Locate every Plasmodium ovale-infected red blood cell.
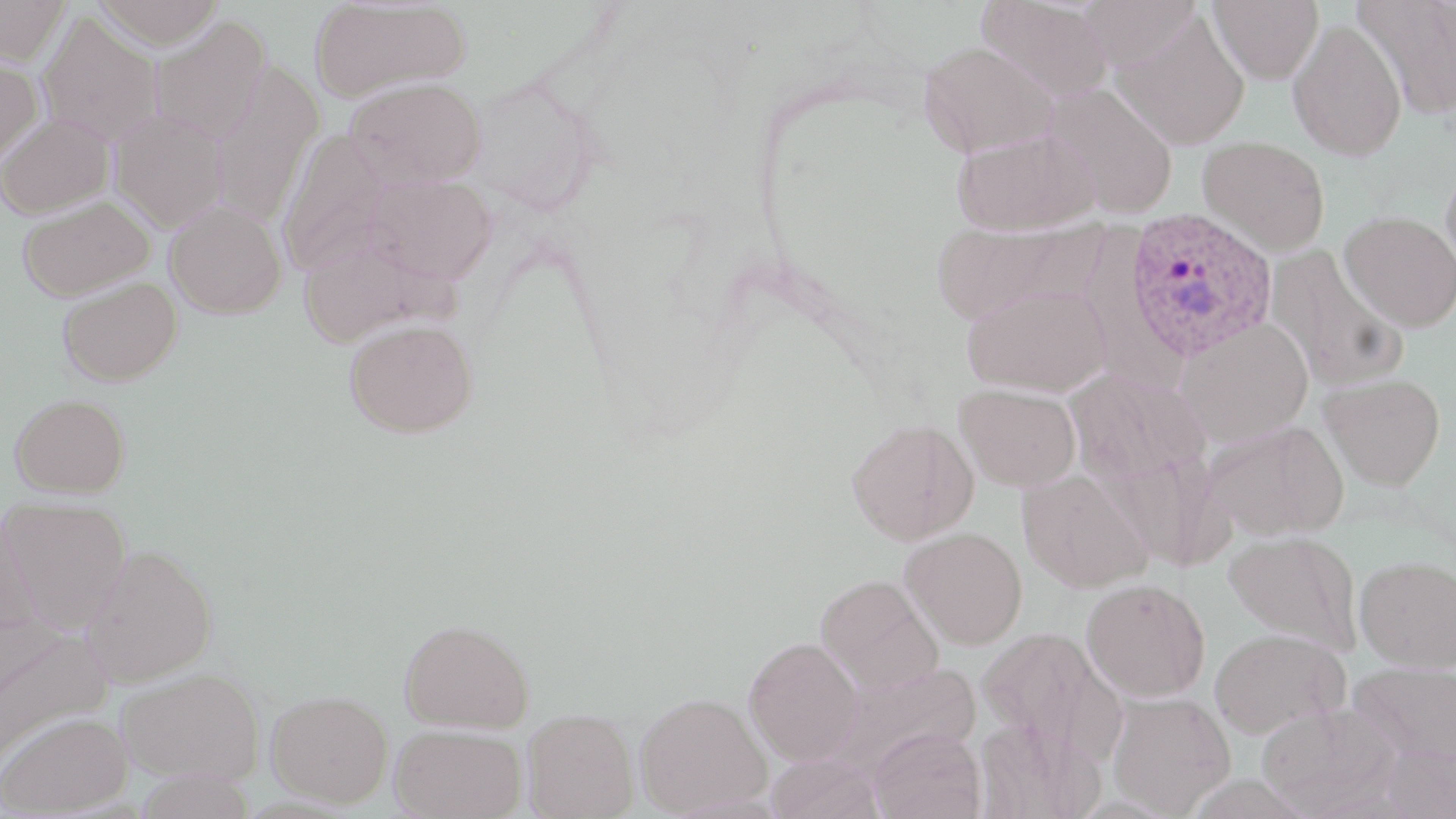
Approximate bounding boxes as (x1, y1, x2, y2) in pixels.
Plasmodium ovale-infected red blood cells: (1123, 207, 1277, 361).

Summary:
  - Uninfected red blood cell locations: (1, 0, 71, 66), (93, 0, 224, 49), (310, 0, 470, 103), (975, 0, 1114, 102), (1209, 0, 1324, 84), (1353, 0, 1456, 121), (1079, 1, 1203, 72), (1111, 10, 1250, 150), (39, 11, 162, 146), (148, 15, 271, 145), (1287, 19, 1407, 161), (918, 40, 1057, 157), (0, 57, 43, 166), (208, 61, 323, 228), (466, 76, 599, 215), (346, 77, 486, 188), (1043, 83, 1179, 219), (111, 108, 228, 233), (0, 113, 114, 219), (277, 128, 391, 276), (952, 128, 1099, 236), (1198, 136, 1330, 255), (1441, 154, 1456, 284), (366, 173, 498, 284), (17, 195, 154, 301), (165, 199, 287, 318), (1340, 211, 1456, 331), (931, 218, 1108, 325), (297, 231, 455, 348), (1267, 245, 1407, 392), (58, 277, 182, 386), (962, 283, 1110, 398), (1175, 317, 1313, 446), (344, 318, 478, 438), (1066, 367, 1212, 496), (1319, 373, 1446, 490), (955, 383, 1081, 491), (10, 394, 130, 497), (846, 418, 979, 545), (1203, 418, 1349, 541), (1018, 469, 1153, 592), (1, 497, 132, 631), (0, 505, 41, 636), (900, 527, 1027, 649), (1224, 530, 1362, 654), (82, 544, 217, 688), (1354, 555, 1456, 672), (815, 575, 943, 696), (1081, 578, 1210, 701), (400, 619, 534, 733), (976, 626, 1117, 754), (1209, 627, 1349, 738), (1, 628, 112, 768), (743, 637, 866, 765), (1348, 662, 1456, 767), (828, 663, 982, 779), (117, 667, 264, 784), (266, 689, 394, 807), (1107, 691, 1236, 815), (635, 692, 771, 816), (1256, 701, 1400, 816), (522, 708, 639, 818), (0, 711, 134, 817), (974, 716, 1094, 818), (390, 723, 527, 819), (870, 727, 985, 819), (1380, 742, 1456, 818), (766, 754, 884, 819)
  - Slide-level diagnosis: Plasmodium ovale
  - Modality: optical microscopy
  - Image size: 1456×819 pixels
  - Field of view: single
  - Magnification: 1000x
  - Preparation: thin blood smear
  - Stain: May-Grünwald-Giemsa